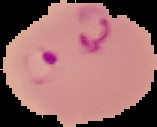
Summary:
  - Malaria status: parasitized
  - Preparation: thin blood smear
  - Image type: segmented cell region with the area outside set to black
  - Image size: 157×127 pixels